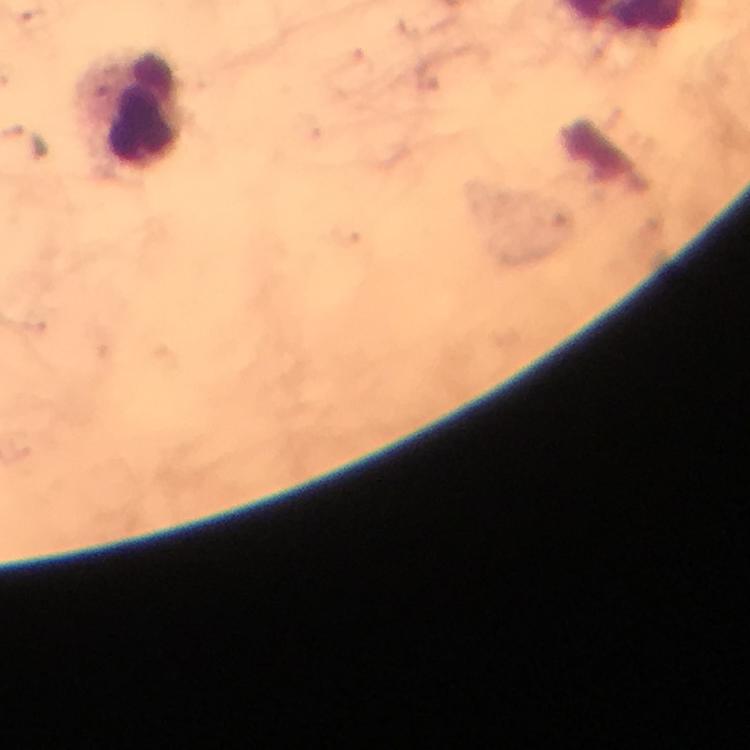
magnification = 100x
malaria parasites = none detected
immersion oil = applied
preparation = thick blood film
stain = Giemsa
context = from a malaria diagnostic workup
image size = 750×750 pixels
leukocyte locations = approximate object centers, in pixels from the top-left corner: (x=132, y=111)
cropped from = one field of view
capture = smartphone mounted on the microscope